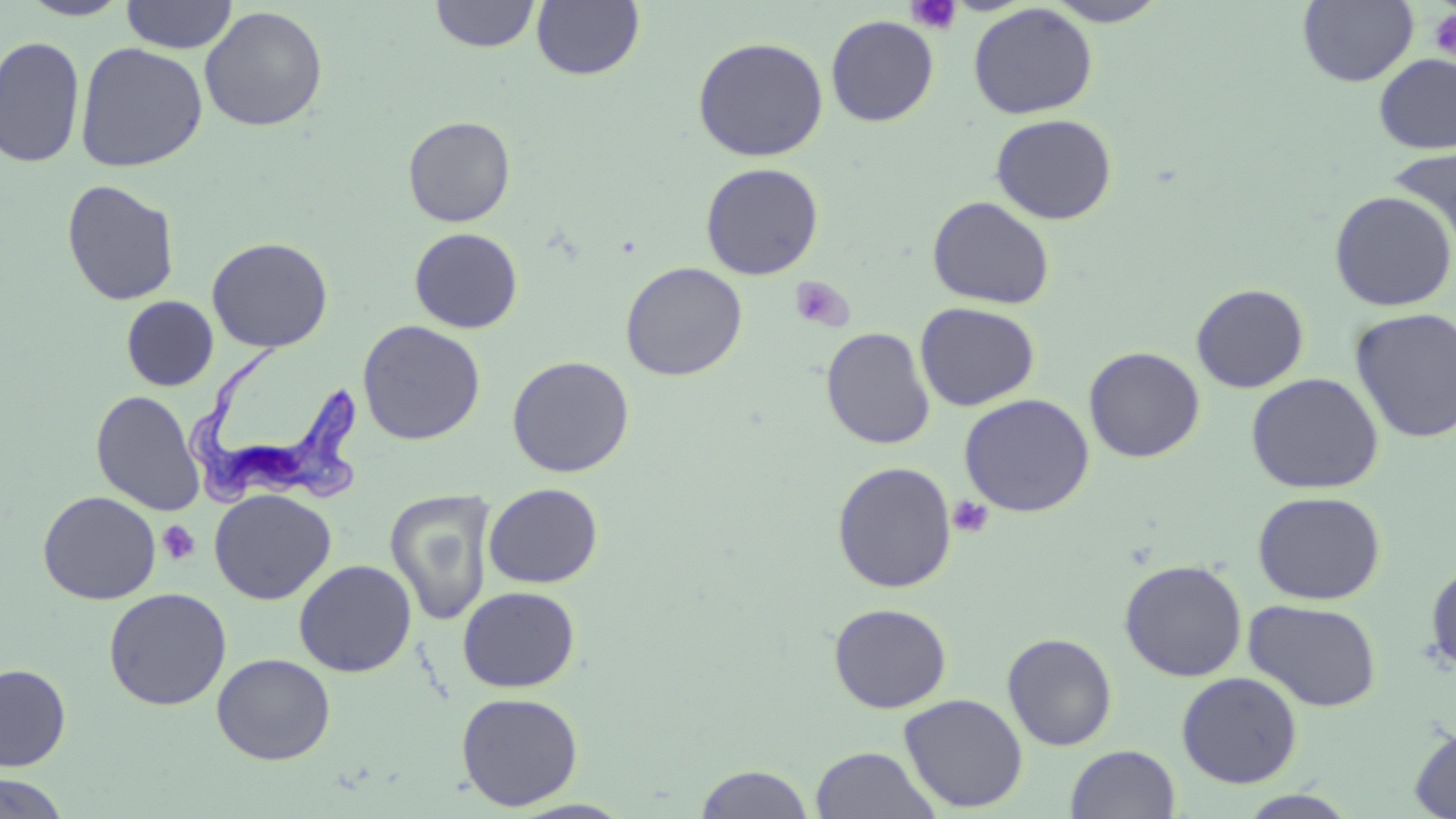 Approximate bounding boxes as (x1,y1)-(x2,y2) corner pairs in pixels. Uninfected red blood cell locations: (17,0)-(134,21), (1042,0)-(1172,27), (1298,0)-(1419,87), (120,1)-(238,53), (429,1)-(540,53), (531,1)-(645,81), (968,3)-(1098,119), (199,5)-(328,132), (826,15)-(939,126), (0,35)-(85,168), (692,36)-(829,162), (74,41)-(209,172), (1373,53)-(1456,153), (990,113)-(1117,225), (402,115)-(516,227), (1386,144)-(1456,255), (700,162)-(824,280), (61,179)-(181,306), (1328,190)-(1456,312), (927,196)-(1055,309), (409,227)-(524,333), (207,236)-(333,353), (620,261)-(748,381), (1191,283)-(1309,393), (121,296)-(218,391), (915,302)-(1040,411), (1349,308)-(1456,443), (356,320)-(486,446), (821,326)-(935,450), (1084,346)-(1205,462), (507,355)-(635,477), (1245,372)-(1384,494), (91,390)-(205,516), (959,393)-(1095,517), (832,461)-(958,593), (484,483)-(603,588), (209,489)-(336,605), (37,490)-(161,605), (385,490)-(495,625), (1253,490)-(1386,605), (294,559)-(417,677), (1119,559)-(1247,681), (1425,560)-(1456,678), (457,586)-(580,692), (103,587)-(232,710), (1244,599)-(1383,712), (828,602)-(952,713), (1002,632)-(1117,751), (212,653)-(336,765), (0,663)-(71,770), (1176,671)-(1303,788), (456,692)-(584,810), (899,693)-(1029,813), (1409,724)-(1456,818), (1066,744)-(1181,819), (810,745)-(941,819), (693,763)-(816,819), (0,772)-(72,818), (1236,790)-(1361,818). Trypanosoma brucei locations: (185,346)-(364,506). Platelet locations: (906,0)-(962,35), (1428,7)-(1456,63), (790,275)-(853,332), (948,494)-(993,537), (157,520)-(201,565). Slide-level diagnosis: Trypanosoma brucei. One field of a larger specimen. Light microscopy. 1000x magnification. May-Grünwald-Giemsa stain. Thin blood film. Image is 1456×819 pixels.